Assess this cell for malaria.
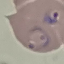
It is parasitized.

Summary:
  - Preparation: thin blood smear
  - Stain: Giemsa
  - Image type: cell patch, automatically extracted from a larger field of view and resized to 64 × 64 pixels
  - Capture: smartphone camera at the microscope eyepiece